Outline each Plasmodium ovale-infected red blood cell.
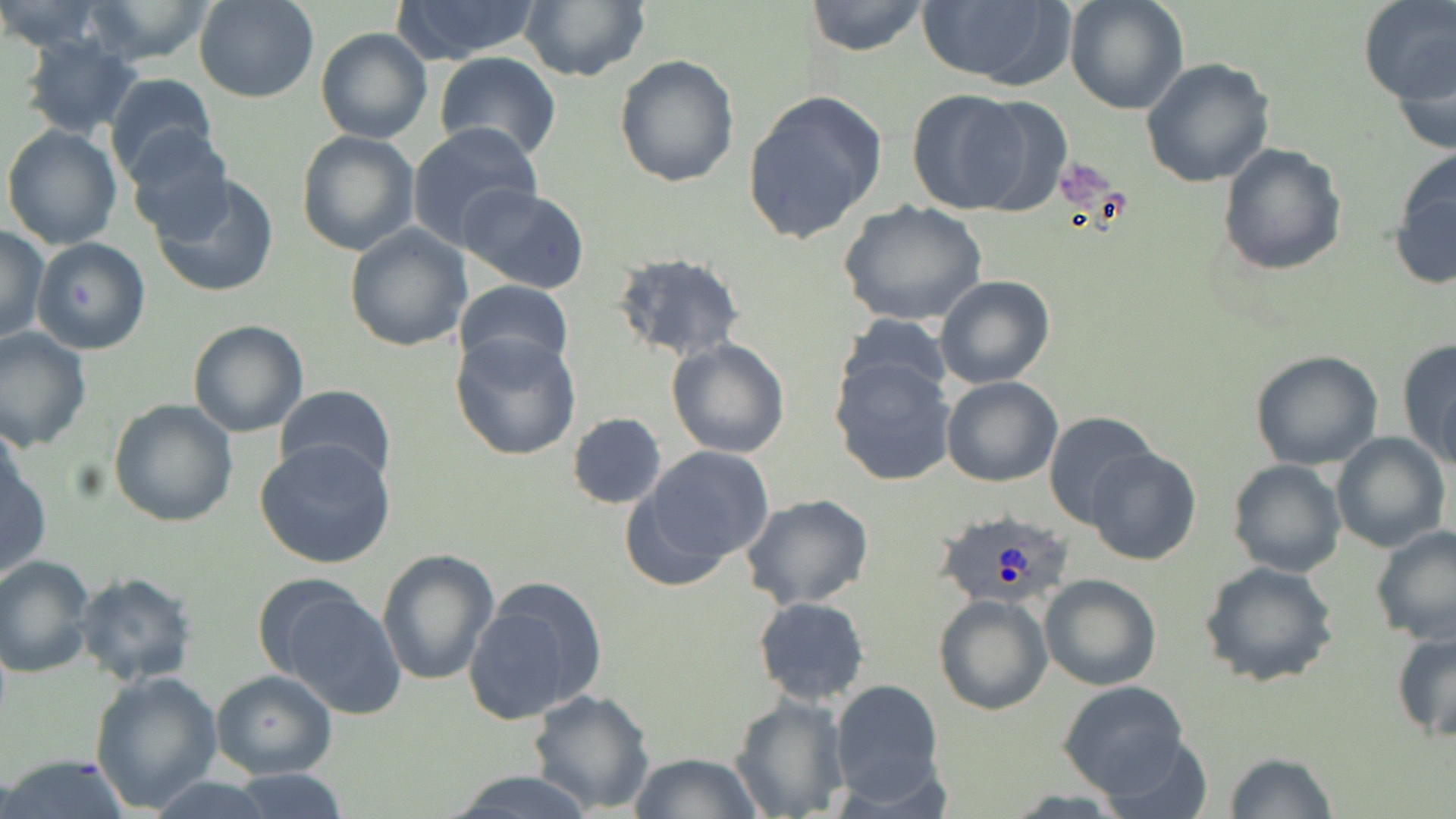

Approximate bounding boxes as (x1, y1, x2, y2) in pixels.
Plasmodium ovale-infected red blood cells: (937, 509, 1070, 609).

Summary:
  - Platelet locations: (1055, 160, 1118, 212)
  - Uninfected red blood cell locations: (81, 0, 219, 66), (193, 0, 320, 103), (392, 0, 542, 62), (520, 0, 650, 84), (805, 0, 929, 57), (1063, 0, 1188, 114), (1358, 0, 1455, 106), (914, 1, 1073, 89), (0, 2, 108, 53), (315, 28, 434, 146), (18, 34, 144, 140), (1389, 42, 1456, 159), (434, 51, 561, 163), (613, 54, 739, 188), (1139, 58, 1277, 189), (105, 73, 219, 185), (905, 88, 1041, 215), (742, 89, 887, 244), (408, 121, 541, 249), (2, 123, 123, 250), (125, 129, 233, 242), (295, 129, 420, 257), (1217, 143, 1347, 275), (1388, 151, 1456, 291), (151, 174, 280, 298), (460, 184, 591, 294), (838, 199, 988, 328), (343, 224, 473, 352), (0, 226, 48, 345), (32, 237, 151, 355), (611, 251, 744, 361), (935, 273, 1055, 389), (454, 279, 573, 374), (836, 312, 953, 409), (188, 320, 309, 438), (0, 326, 92, 452), (451, 332, 582, 461), (1396, 336, 1456, 471), (668, 338, 788, 458), (1249, 350, 1384, 471), (829, 354, 959, 487), (941, 376, 1064, 488), (276, 383, 395, 486), (108, 399, 238, 526), (1044, 411, 1157, 527), (567, 412, 667, 510), (1330, 432, 1450, 553), (254, 439, 397, 571), (635, 445, 777, 575), (1084, 447, 1201, 566), (1, 453, 49, 579), (1226, 458, 1347, 578), (740, 492, 875, 609), (1370, 525, 1456, 644), (376, 549, 500, 687), (0, 555, 98, 677), (1197, 560, 1339, 688), (72, 572, 198, 687), (1039, 574, 1163, 692), (464, 580, 607, 727), (269, 584, 407, 718), (934, 594, 1051, 715), (753, 596, 870, 704), (1390, 628, 1456, 742), (211, 670, 338, 780), (89, 671, 223, 812), (830, 679, 944, 802), (1057, 681, 1190, 796), (526, 687, 656, 813), (729, 693, 852, 819), (1094, 729, 1215, 819), (627, 752, 762, 818), (1224, 752, 1337, 818), (1, 753, 133, 818), (225, 768, 349, 819), (446, 769, 599, 819)
  - Slide-level diagnosis: Plasmodium ovale
  - Preparation: thin blood smear
  - Stain: May-Grünwald-Giemsa
  - Field of view: one of a larger specimen
  - Modality: optical microscopy
  - Magnification: 1000x
  - Image size: 1456×819 pixels